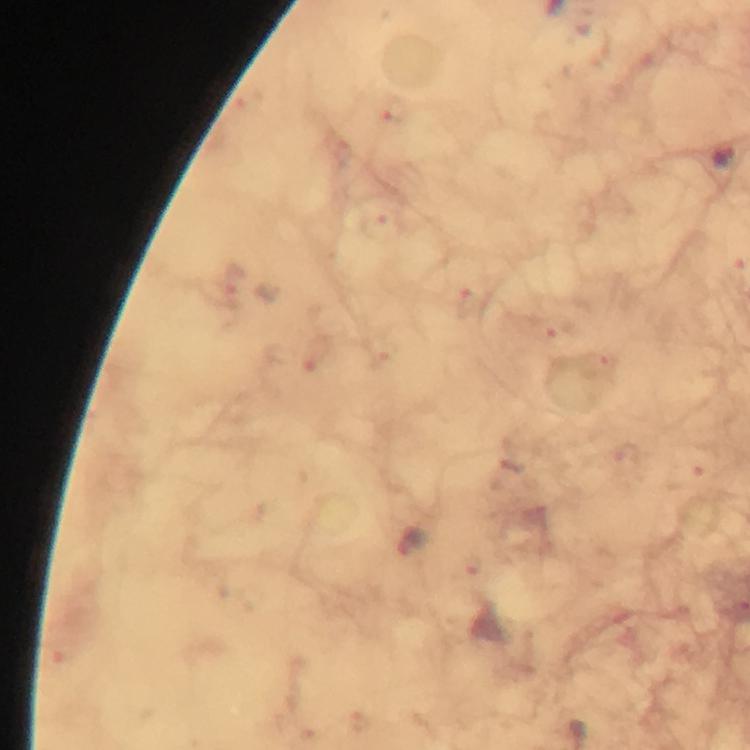
stain: Giemsa
image_size: 750×750 pixels
magnification: 100x
malaria_parasite_locations: 'approximate centers as (x, y) in pixels: (411, 542)'
preparation: thick smear
capture: smartphone camera through the microscope
cropped_from: one field of view
context: from a diagnostic examination for malaria
immersion_oil: applied